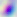

identification: Toxoplasma gondii
magnification: 400x
modality: micrograph